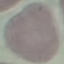
Summary:
  - Result: negative for malaria parasites
  - Preparation: thin blood smear
  - Image type: cell patch, automatically extracted from a larger field of view and resized to 64 × 64 pixels
  - Stain: Giemsa
  - Capture: smartphone through the microscope eyepiece